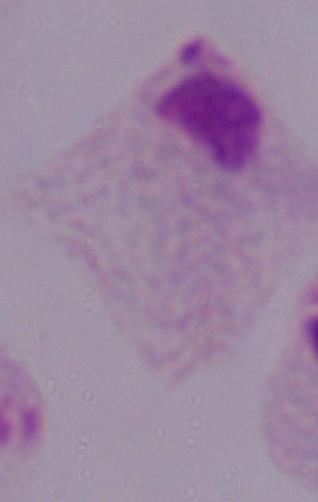
modality = photomicrograph
identification = trichomonad
magnification = 1000x